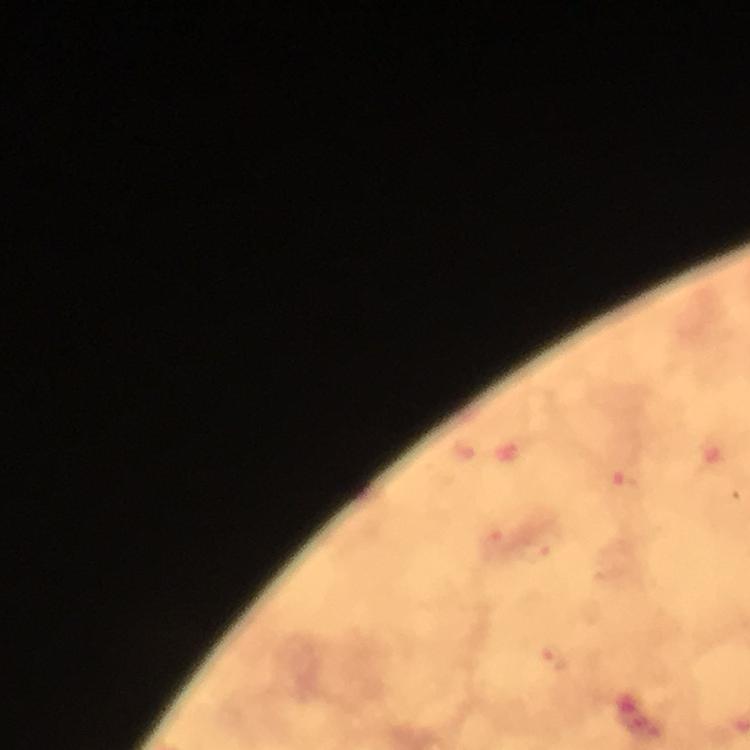

Approximate object centers, in pixels from the top-left corner. Malaria parasite locations: (x=620, y=481), (x=496, y=540), (x=542, y=549), (x=554, y=659). From a malaria diagnostic workup. Immersion oil applied. Giemsa stain. Cropped region of a single field of view. Image is 750×750 pixels. 100x magnification. Thick blood smear. Photographed through the microscope with a smartphone camera.